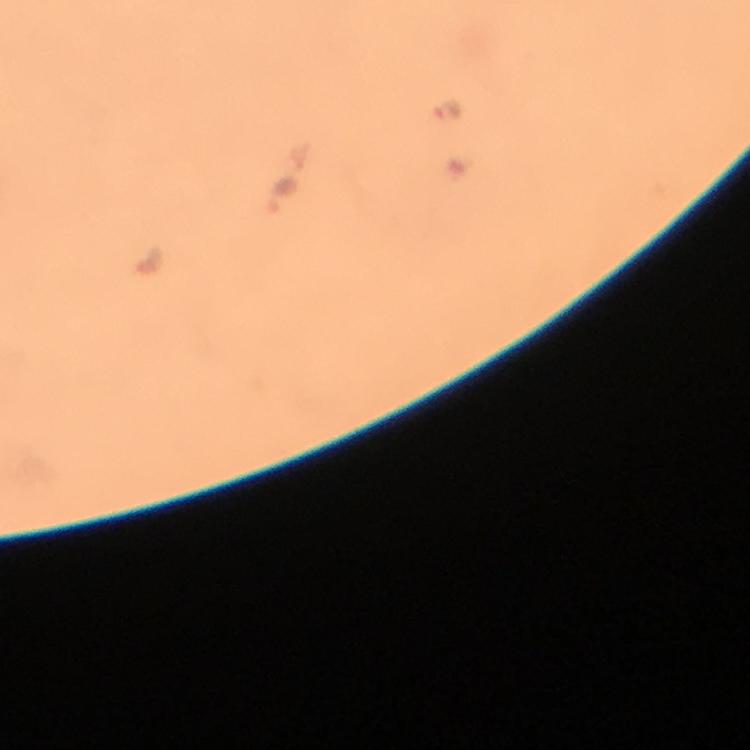

Approximate centers as {x, y} in pixels.
Summary:
  - Malaria parasite locations: {445, 110}, {280, 194}
  - Magnification: 100x
  - Stain: Giemsa
  - Immersion oil: used
  - Context: from a diagnostic examination for malaria
  - Cropped from: one field of view
  - Preparation: thick smear
  - Image size: 750×750 pixels
  - Capture: smartphone camera through the microscope